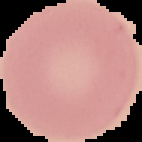

Image is 142×142 pixels. From a thin blood smear. Segmented cell region on a black background. Malaria status: uninfected.